Describe the morphology of the erythrocytes.
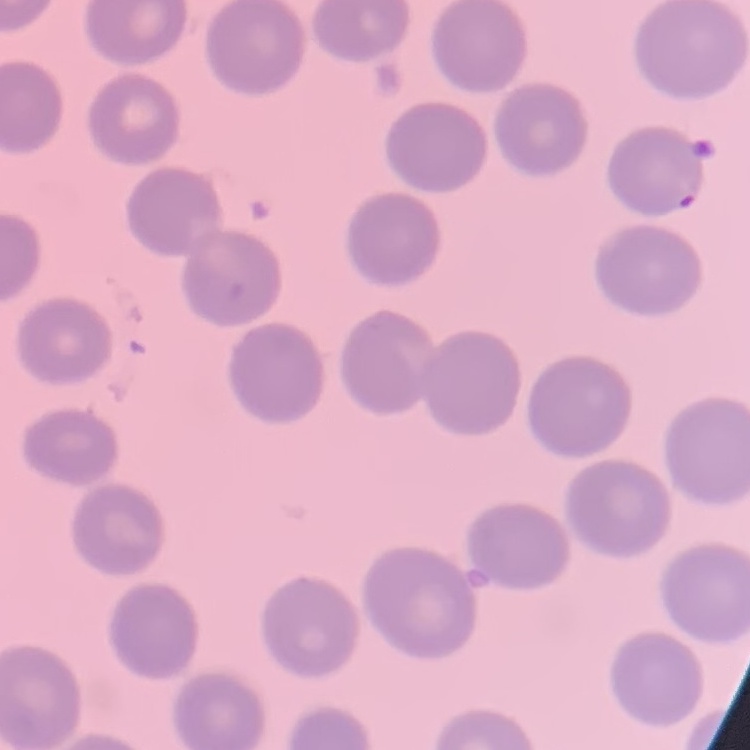
No rouleaux formation.

image type = one tile cut from a larger photomicrograph
preparation = thin blood film
stain = Field's or Giemsa